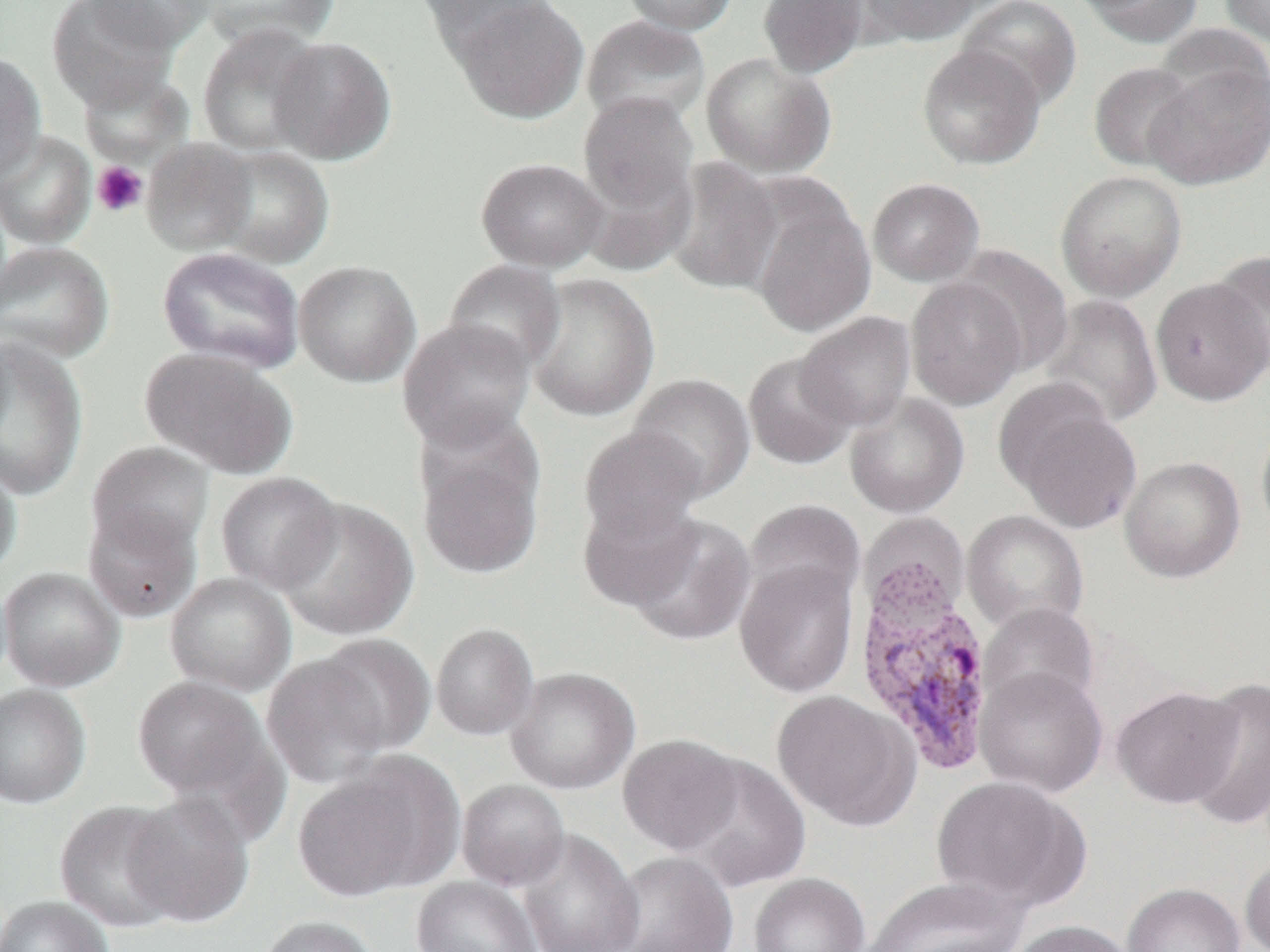

Plasmodium vivax-infected red blood cell locations = approximate bounding boxes as named x1/y1/x2/y2 corners in pixels: (x1=852, y1=563, x2=997, y2=777)
slide-level diagnosis = Plasmodium vivax
platelet locations = approximate bounding boxes as named x1/y1/x2/y2 corners in pixels: (x1=92, y1=161, x2=148, y2=218)
preparation = thin blood smear
modality = light microscopy
uninfected red blood cell locations = approximate bounding boxes as named x1/y1/x2/y2 corners in pixels: (x1=46, y1=0, x2=181, y2=113), (x1=84, y1=0, x2=215, y2=52), (x1=194, y1=0, x2=341, y2=50), (x1=416, y1=0, x2=558, y2=60), (x1=449, y1=0, x2=590, y2=123), (x1=620, y1=0, x2=737, y2=35), (x1=758, y1=0, x2=869, y2=78), (x1=854, y1=0, x2=986, y2=48), (x1=956, y1=0, x2=1083, y2=110), (x1=1076, y1=0, x2=1205, y2=48), (x1=1219, y1=0, x2=1270, y2=48), (x1=580, y1=14, x2=711, y2=128), (x1=196, y1=23, x2=326, y2=156), (x1=268, y1=36, x2=396, y2=165), (x1=917, y1=42, x2=1047, y2=170), (x1=0, y1=52, x2=47, y2=184), (x1=700, y1=52, x2=836, y2=178), (x1=1143, y1=60, x2=1270, y2=189), (x1=1087, y1=61, x2=1202, y2=173), (x1=578, y1=91, x2=700, y2=215), (x1=0, y1=130, x2=96, y2=250), (x1=141, y1=139, x2=257, y2=255), (x1=207, y1=145, x2=334, y2=268), (x1=476, y1=157, x2=609, y2=272), (x1=665, y1=157, x2=783, y2=296), (x1=1055, y1=170, x2=1187, y2=302), (x1=867, y1=177, x2=985, y2=286), (x1=749, y1=192, x2=876, y2=337), (x1=0, y1=241, x2=115, y2=363), (x1=953, y1=245, x2=1074, y2=375), (x1=156, y1=246, x2=305, y2=373), (x1=1210, y1=252, x2=1270, y2=374), (x1=441, y1=258, x2=566, y2=375), (x1=294, y1=260, x2=421, y2=387), (x1=524, y1=272, x2=660, y2=422), (x1=905, y1=276, x2=1028, y2=411), (x1=1150, y1=278, x2=1270, y2=405), (x1=1040, y1=294, x2=1163, y2=428), (x1=795, y1=311, x2=917, y2=432), (x1=398, y1=318, x2=536, y2=451), (x1=0, y1=337, x2=88, y2=500), (x1=140, y1=347, x2=298, y2=479), (x1=742, y1=351, x2=859, y2=471), (x1=626, y1=373, x2=755, y2=501), (x1=844, y1=392, x2=970, y2=519), (x1=1005, y1=395, x2=1142, y2=533), (x1=1255, y1=416, x2=1270, y2=542), (x1=578, y1=425, x2=709, y2=546), (x1=416, y1=438, x2=544, y2=579), (x1=86, y1=441, x2=216, y2=557), (x1=1119, y1=456, x2=1246, y2=583), (x1=0, y1=458, x2=21, y2=579), (x1=216, y1=471, x2=343, y2=593), (x1=274, y1=497, x2=420, y2=641), (x1=577, y1=498, x2=703, y2=611), (x1=744, y1=498, x2=866, y2=610), (x1=83, y1=504, x2=201, y2=623), (x1=962, y1=510, x2=1089, y2=635), (x1=625, y1=513, x2=757, y2=646), (x1=734, y1=558, x2=860, y2=698), (x1=0, y1=566, x2=126, y2=692), (x1=165, y1=572, x2=297, y2=697), (x1=978, y1=602, x2=1100, y2=716), (x1=431, y1=622, x2=539, y2=741), (x1=312, y1=633, x2=437, y2=755), (x1=261, y1=653, x2=392, y2=789), (x1=975, y1=666, x2=1108, y2=798), (x1=505, y1=667, x2=640, y2=794), (x1=131, y1=675, x2=275, y2=803), (x1=1184, y1=676, x2=1270, y2=829), (x1=0, y1=683, x2=92, y2=809), (x1=1111, y1=685, x2=1244, y2=809), (x1=771, y1=689, x2=920, y2=831), (x1=617, y1=733, x2=744, y2=855), (x1=676, y1=754, x2=811, y2=892), (x1=292, y1=761, x2=448, y2=902), (x1=930, y1=775, x2=1089, y2=912), (x1=456, y1=779, x2=570, y2=891), (x1=123, y1=791, x2=255, y2=928), (x1=54, y1=800, x2=185, y2=933), (x1=516, y1=828, x2=644, y2=952), (x1=608, y1=850, x2=739, y2=952), (x1=1240, y1=855, x2=1270, y2=952), (x1=748, y1=872, x2=870, y2=952), (x1=411, y1=876, x2=541, y2=952), (x1=862, y1=876, x2=1028, y2=952), (x1=1122, y1=882, x2=1246, y2=952), (x1=0, y1=895, x2=114, y2=952), (x1=256, y1=915, x2=381, y2=952), (x1=1008, y1=920, x2=1138, y2=952)
image size = 1270×952 pixels
field of view = one of a larger specimen
magnification = 1000x